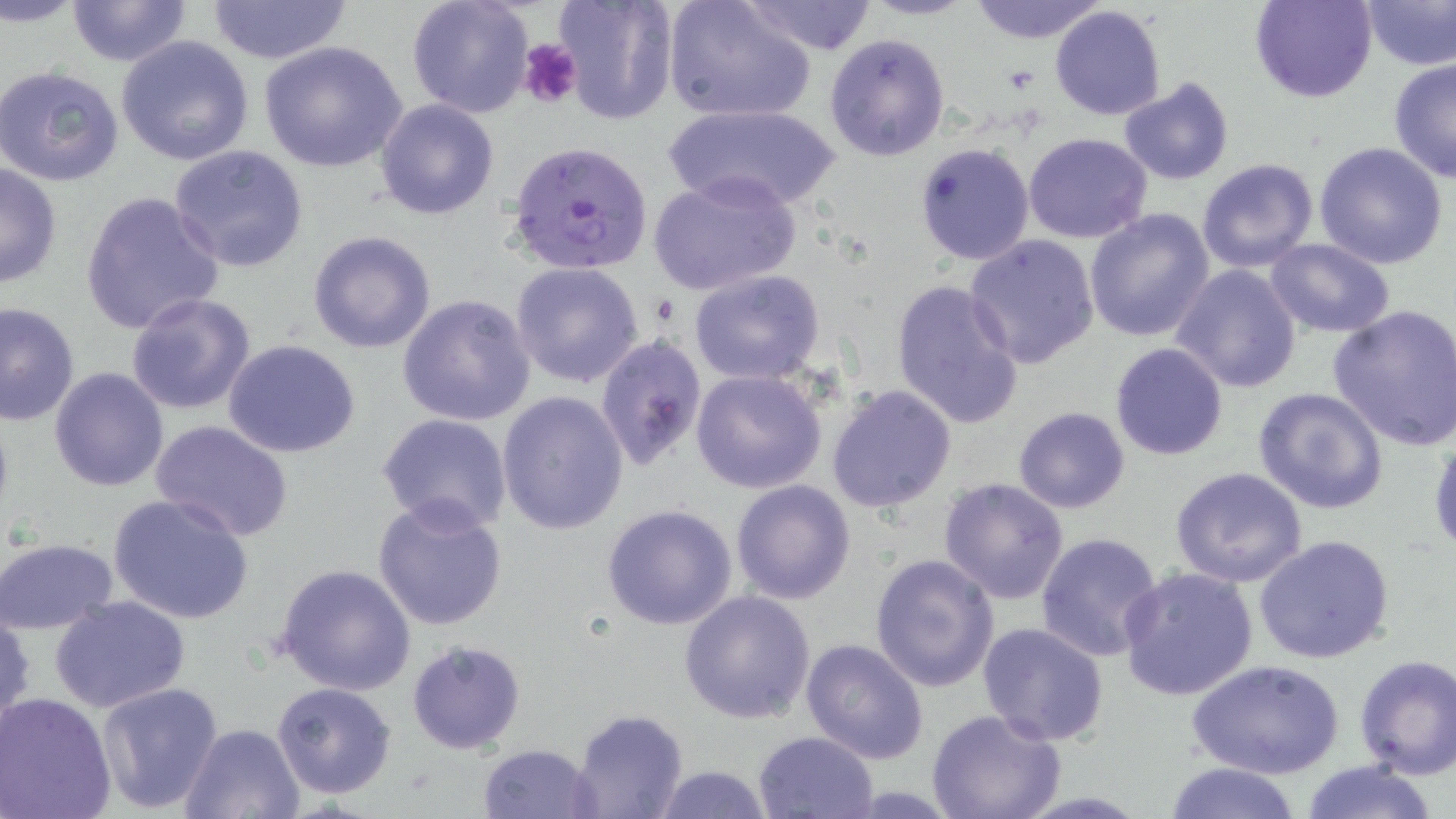

Summary:
  - Coordinate format: approximate bounding boxes as named x1/y1/x2/y2 corners in pixels
  - Plasmodium falciparum-infected red blood cell locations: (x1=508, y1=138, x2=654, y2=274)
  - Uninfected red blood cell locations: (x1=65, y1=0, x2=196, y2=67), (x1=206, y1=0, x2=355, y2=66), (x1=406, y1=0, x2=535, y2=119), (x1=555, y1=0, x2=678, y2=124), (x1=738, y1=0, x2=880, y2=55), (x1=864, y1=0, x2=976, y2=21), (x1=968, y1=0, x2=1108, y2=44), (x1=1251, y1=0, x2=1377, y2=103), (x1=663, y1=1, x2=815, y2=123), (x1=1361, y1=1, x2=1456, y2=71), (x1=1050, y1=4, x2=1167, y2=122), (x1=824, y1=33, x2=950, y2=160), (x1=116, y1=36, x2=255, y2=165), (x1=259, y1=40, x2=410, y2=174), (x1=1389, y1=57, x2=1456, y2=183), (x1=1, y1=65, x2=125, y2=187), (x1=1118, y1=78, x2=1235, y2=184), (x1=374, y1=99, x2=500, y2=221), (x1=661, y1=102, x2=843, y2=212), (x1=1023, y1=132, x2=1151, y2=242), (x1=914, y1=142, x2=1034, y2=266), (x1=1313, y1=142, x2=1449, y2=269), (x1=169, y1=144, x2=309, y2=272), (x1=1197, y1=159, x2=1320, y2=274), (x1=0, y1=162, x2=62, y2=287), (x1=647, y1=170, x2=803, y2=299), (x1=78, y1=191, x2=226, y2=337), (x1=1085, y1=207, x2=1216, y2=343), (x1=307, y1=231, x2=436, y2=353), (x1=962, y1=234, x2=1101, y2=371), (x1=1263, y1=238, x2=1395, y2=337), (x1=509, y1=262, x2=645, y2=388), (x1=1170, y1=263, x2=1303, y2=393), (x1=688, y1=270, x2=826, y2=385), (x1=891, y1=278, x2=1024, y2=429), (x1=126, y1=292, x2=257, y2=414), (x1=397, y1=294, x2=535, y2=427), (x1=0, y1=300, x2=80, y2=427), (x1=1327, y1=304, x2=1456, y2=451), (x1=595, y1=333, x2=707, y2=473), (x1=224, y1=340, x2=363, y2=459), (x1=1109, y1=342, x2=1228, y2=460), (x1=48, y1=366, x2=170, y2=492), (x1=691, y1=369, x2=827, y2=494), (x1=827, y1=383, x2=957, y2=513), (x1=1251, y1=386, x2=1391, y2=516), (x1=497, y1=391, x2=628, y2=535), (x1=1012, y1=406, x2=1131, y2=513), (x1=376, y1=414, x2=514, y2=534), (x1=150, y1=417, x2=296, y2=542), (x1=1427, y1=433, x2=1456, y2=556), (x1=1170, y1=467, x2=1309, y2=587), (x1=938, y1=477, x2=1070, y2=604), (x1=731, y1=480, x2=856, y2=604), (x1=108, y1=492, x2=257, y2=626), (x1=373, y1=496, x2=509, y2=632), (x1=602, y1=504, x2=737, y2=631), (x1=1034, y1=531, x2=1166, y2=663), (x1=1253, y1=534, x2=1395, y2=664), (x1=0, y1=536, x2=119, y2=635), (x1=93, y1=539, x2=234, y2=689), (x1=869, y1=554, x2=1000, y2=692), (x1=275, y1=563, x2=416, y2=695), (x1=1118, y1=566, x2=1258, y2=701), (x1=680, y1=590, x2=817, y2=723), (x1=50, y1=594, x2=190, y2=714), (x1=0, y1=609, x2=35, y2=739), (x1=977, y1=623, x2=1109, y2=746), (x1=801, y1=638, x2=930, y2=765), (x1=406, y1=639, x2=527, y2=753), (x1=1354, y1=654, x2=1456, y2=780), (x1=1188, y1=659, x2=1344, y2=781), (x1=94, y1=680, x2=223, y2=814), (x1=272, y1=682, x2=398, y2=801), (x1=0, y1=693, x2=118, y2=819), (x1=570, y1=707, x2=688, y2=819), (x1=927, y1=710, x2=1065, y2=819), (x1=179, y1=722, x2=306, y2=819), (x1=753, y1=730, x2=878, y2=818), (x1=478, y1=743, x2=602, y2=818), (x1=1299, y1=759, x2=1439, y2=819), (x1=1161, y1=760, x2=1305, y2=818), (x1=647, y1=763, x2=773, y2=819)
  - Platelet locations: (x1=518, y1=37, x2=581, y2=112)
  - Slide-level diagnosis: Plasmodium falciparum
  - Modality: optical microscopy
  - Field of view: single
  - Image size: 1456×819 pixels
  - Stain: May-Grünwald-Giemsa
  - Preparation: thin blood film
  - Magnification: 1000x